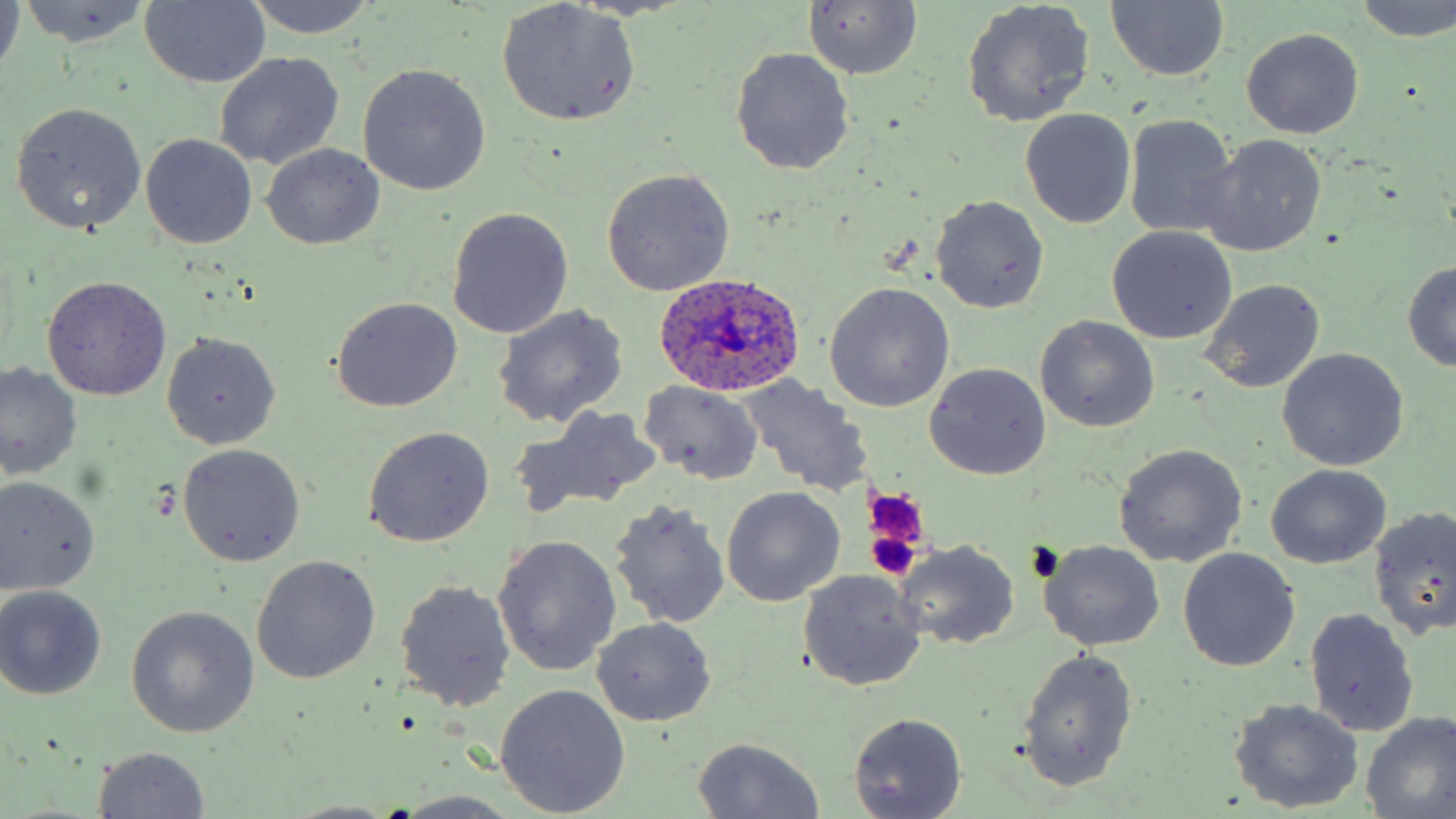
Approximate bounding boxes as (x1,y1)-(x2,y2) corner pairs in pixels. Uninfected red blood cell locations: (0,0)-(24,79), (242,0)-(377,38), (803,0)-(924,80), (1106,0)-(1228,84), (15,1)-(151,47), (497,1)-(641,126), (1353,1)-(1456,41), (140,2)-(270,88), (962,2)-(1096,127), (1241,29)-(1364,140), (729,46)-(854,176), (214,51)-(345,171), (357,63)-(491,196), (10,102)-(147,234), (1020,108)-(1136,229), (1124,115)-(1239,238), (141,134)-(258,249), (1198,135)-(1328,257), (260,143)-(384,249), (600,168)-(735,297), (931,196)-(1048,313), (447,207)-(573,339), (1107,227)-(1237,345), (1401,260)-(1456,372), (43,276)-(171,400), (1200,280)-(1326,395), (826,283)-(954,412), (331,297)-(463,413), (491,303)-(628,429), (1035,316)-(1160,434), (162,334)-(280,450), (1276,347)-(1409,472), (925,362)-(1051,480), (0,363)-(80,482), (737,376)-(871,500), (639,381)-(763,486), (525,404)-(660,513), (362,427)-(495,548), (178,443)-(305,566), (1113,445)-(1245,569), (1266,465)-(1391,568), (0,477)-(101,597), (721,487)-(846,608), (608,499)-(729,629), (1369,505)-(1456,642), (492,535)-(622,676), (895,541)-(1020,650), (1041,542)-(1164,652), (1179,548)-(1300,672), (251,555)-(380,685), (797,569)-(928,691), (394,579)-(517,712), (0,585)-(107,700), (126,606)-(260,739), (1303,608)-(1420,738), (592,618)-(715,726), (1014,647)-(1139,793), (496,685)-(630,816), (1231,699)-(1365,813), (847,712)-(968,819), (1359,713)-(1455,817), (691,736)-(825,818), (93,746)-(210,818), (389,792)-(527,817), (283,800)-(401,818). Platelet locations: (863,487)-(933,553), (867,529)-(923,582). Plasmodium ovale-infected red blood cell locations: (653,272)-(808,396). Slide-level diagnosis: Plasmodium ovale. Image is 1456×819 pixels. Optical microscopy. May-Grünwald-Giemsa stain. One field of a larger specimen. 1000x magnification. Thin blood film.